Assess this cell for malaria.
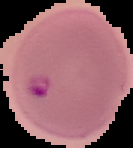

It is parasitized.

Summary:
  - Image type: cell region segmented out of the field of view; surrounding area masked to black
  - Preparation: thin blood film
  - Image size: 133×148 pixels